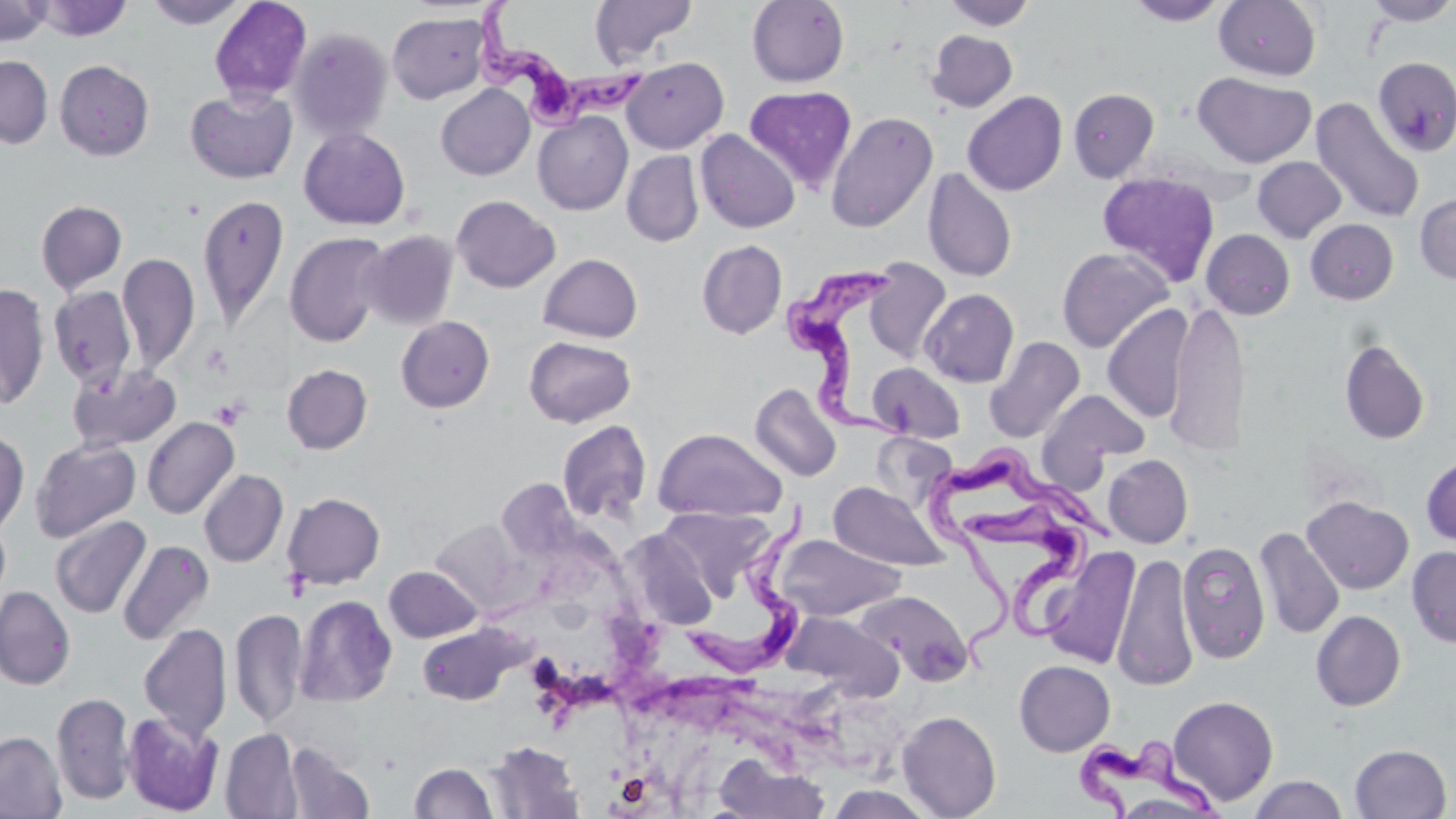

Trypanosoma brucei locations = approximate bounding boxes as [x1, y1, x2, y2] in pixels: [475, 0, 649, 139], [780, 262, 909, 446], [930, 442, 1113, 682], [680, 501, 816, 680], [968, 502, 1089, 643], [1077, 734, 1219, 817]
slide-level diagnosis = Trypanosoma brucei
modality = light microscopy
field of view = one of a larger specimen
platelet locations = approximate bounding boxes as [x1, y1, x2, y2] in pixels: [201, 344, 230, 378], [211, 397, 247, 429], [282, 568, 312, 601]
stain = May-Grünwald-Giemsa
preparation = thin blood film
magnification = 1000x
uninfected red blood cell locations = approximate bounding boxes as [x1, y1, x2, y2] in pixels: [33, 0, 132, 41], [144, 0, 249, 29], [209, 0, 312, 103], [590, 0, 696, 65], [747, 0, 849, 87], [1128, 0, 1230, 25], [1214, 0, 1321, 81], [1363, 0, 1456, 26], [0, 1, 52, 46], [940, 1, 1037, 30], [387, 11, 490, 104], [289, 27, 393, 143], [926, 30, 1017, 112], [0, 55, 53, 149], [622, 56, 728, 153], [1373, 57, 1455, 156], [55, 60, 154, 161], [1193, 72, 1315, 168], [436, 84, 534, 180], [744, 85, 857, 192], [185, 87, 297, 184], [1068, 88, 1159, 182], [962, 90, 1068, 196], [1310, 97, 1425, 225], [533, 111, 633, 215], [825, 111, 938, 232], [299, 127, 410, 230], [696, 129, 800, 233], [622, 151, 703, 247], [1252, 156, 1347, 243], [923, 167, 1018, 282], [1096, 171, 1220, 286], [1414, 192, 1456, 285], [197, 194, 290, 331], [451, 195, 560, 293], [36, 200, 127, 295], [1305, 218, 1399, 304], [1201, 228, 1295, 319], [359, 230, 459, 330], [285, 232, 390, 347], [697, 240, 787, 339], [1056, 247, 1174, 352], [117, 252, 200, 374], [538, 253, 643, 342], [862, 258, 951, 363], [0, 283, 50, 409], [49, 286, 137, 388], [919, 288, 1019, 388], [1167, 301, 1249, 458], [1102, 304, 1193, 423], [396, 316, 495, 413], [524, 336, 636, 427], [983, 336, 1085, 443], [1338, 338, 1431, 445], [868, 362, 965, 442], [69, 364, 182, 452], [282, 364, 372, 454], [749, 382, 843, 483], [1040, 388, 1151, 473], [142, 416, 239, 519], [557, 419, 652, 524], [652, 427, 788, 523], [0, 428, 29, 537], [30, 438, 141, 542], [1103, 454, 1193, 548], [1421, 454, 1456, 549], [199, 469, 288, 567], [827, 482, 950, 571], [282, 492, 385, 589], [1302, 496, 1414, 594], [656, 507, 777, 602], [50, 515, 150, 619], [430, 518, 530, 616], [1253, 526, 1345, 640], [620, 529, 720, 629], [774, 534, 905, 620], [118, 540, 214, 645], [1177, 541, 1271, 663], [1406, 545, 1456, 649], [1040, 547, 1141, 668], [1112, 552, 1199, 691], [384, 566, 482, 642], [0, 586, 75, 690], [854, 589, 973, 686], [295, 595, 397, 707], [230, 608, 306, 729], [781, 610, 902, 701], [1311, 610, 1406, 711], [139, 623, 232, 741], [418, 624, 521, 706], [1014, 660, 1115, 756], [51, 692, 135, 805], [1167, 695, 1278, 805], [897, 710, 1002, 819], [121, 711, 224, 815], [221, 728, 302, 818], [0, 731, 66, 819], [487, 741, 585, 818], [285, 742, 375, 819], [1350, 744, 1452, 819], [714, 752, 830, 819], [409, 762, 497, 818], [1248, 775, 1348, 818], [825, 784, 939, 819]
image size = 1456×819 pixels